Classify this cell by malaria status.
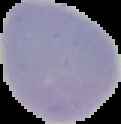

It is uninfected.

The area outside the segmented cell region is set to black. Image is 121×124 pixels. From a thin blood film.